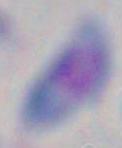

identification = Toxoplasma gondii
modality = micrograph
magnification = 1000x